Report the malaria status of this cell.
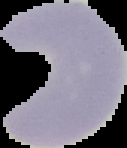
It is uninfected.

Summary:
  - Image type: cell region segmented out of the field of view; surrounding area masked to black
  - Image size: 127×148 pixels
  - Preparation: thin blood film